Assess this cell for malaria.
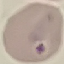

It is uninfected.

Summary:
  - Stain: Giemsa
  - Capture: smartphone through the microscope eyepiece
  - Image type: cell patch, automatically extracted from a larger field of view and resized to 64 × 64 pixels
  - Preparation: thin smear